Outline each blood parasite and name the species.
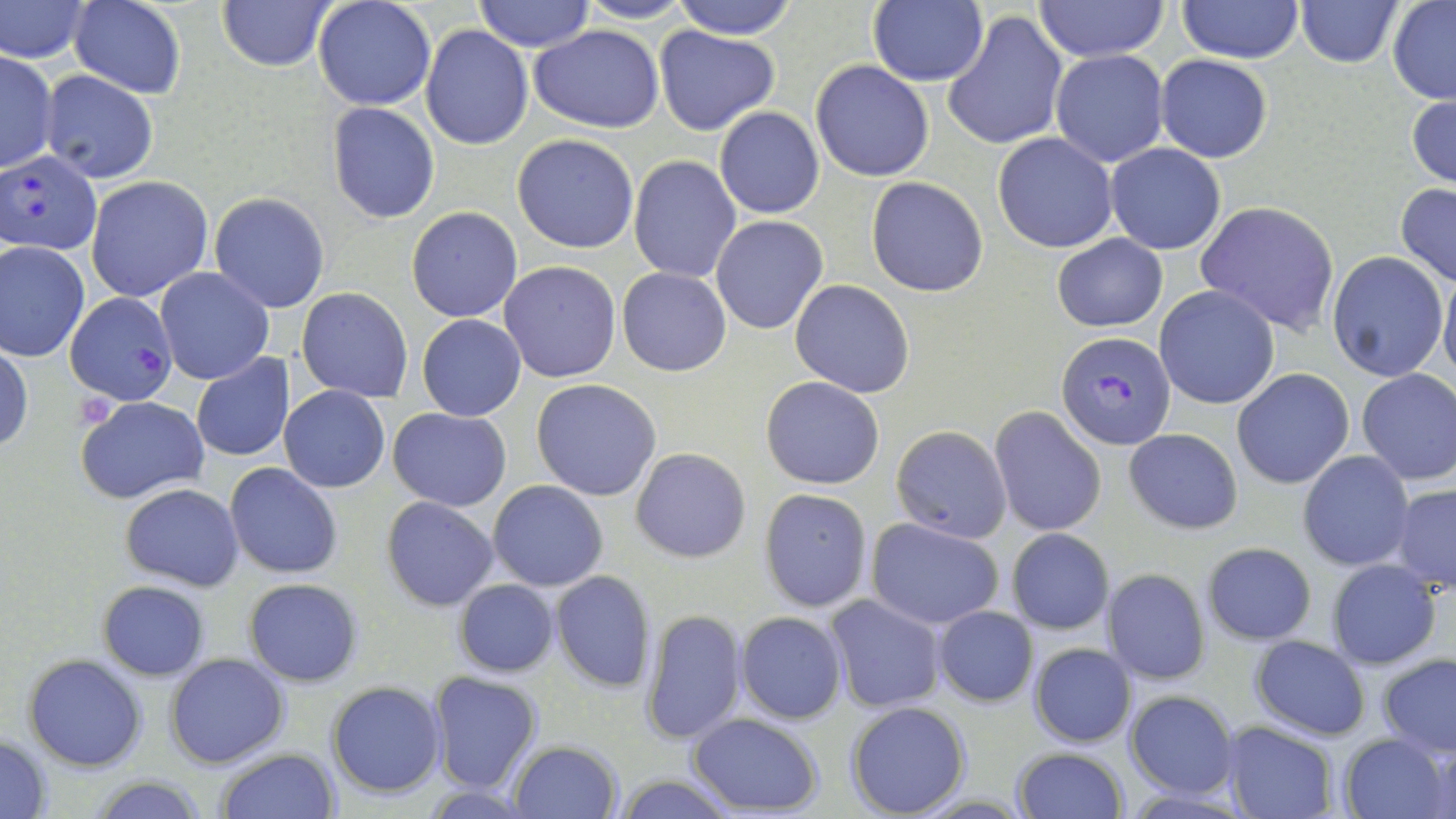
Approximate bounding boxes as (x1, y1, x2, y2) in pixels.
Plasmodium falciparum-infected red blood cells: (0, 150, 102, 255), (66, 292, 177, 406), (1057, 332, 1175, 450).
No Plasmodium ovale, Plasmodium malariae, Plasmodium vivax, Babesia divergens, or Trypanosoma brucei observed.

Uninfected red blood cell locations: (217, 0, 336, 73), (312, 0, 436, 110), (474, 0, 594, 52), (574, 0, 698, 23), (668, 0, 801, 40), (1296, 0, 1401, 68), (1386, 0, 1456, 104), (0, 1, 94, 62), (68, 1, 185, 97), (1032, 1, 1169, 63), (1177, 1, 1305, 63), (867, 2, 990, 87), (943, 10, 1068, 152), (422, 25, 534, 149), (529, 26, 664, 133), (655, 26, 779, 135), (1, 49, 58, 174), (1050, 50, 1170, 167), (1155, 54, 1272, 163), (810, 59, 935, 182), (40, 70, 160, 184), (1407, 89, 1456, 191), (326, 103, 440, 223), (714, 106, 824, 219), (512, 134, 640, 254), (992, 134, 1118, 253), (1106, 143, 1226, 254), (629, 155, 741, 283), (86, 176, 214, 303), (866, 176, 990, 296), (1395, 182, 1456, 287), (209, 193, 329, 312), (1194, 200, 1341, 335), (406, 206, 523, 322), (711, 215, 828, 335), (1169, 232, 1317, 397), (1053, 233, 1167, 332), (0, 240, 90, 361), (1326, 251, 1449, 382), (497, 261, 623, 383), (1439, 263, 1456, 384), (618, 266, 731, 377), (156, 267, 274, 385), (791, 279, 914, 397), (1154, 285, 1280, 409), (297, 287, 415, 403), (417, 314, 526, 421), (0, 343, 33, 455), (191, 355, 295, 462), (1356, 367, 1455, 487), (1232, 368, 1355, 489), (760, 376, 885, 489), (531, 379, 661, 501), (279, 386, 390, 492), (75, 394, 209, 505), (990, 406, 1107, 538), (387, 409, 512, 509), (890, 424, 1013, 543), (1124, 429, 1243, 534), (630, 447, 751, 562), (1298, 450, 1414, 572), (226, 463, 343, 580), (487, 480, 608, 592), (119, 482, 245, 591), (1389, 484, 1456, 595), (759, 489, 872, 612), (381, 496, 500, 612), (866, 518, 1003, 630), (1007, 528, 1114, 634), (1200, 542, 1316, 644), (1326, 559, 1442, 670), (1101, 568, 1211, 684), (550, 570, 656, 691), (242, 577, 364, 687), (453, 579, 559, 677), (97, 581, 209, 681), (824, 596, 946, 713), (933, 606, 1037, 707), (639, 608, 748, 744), (735, 611, 847, 724), (1250, 637, 1370, 740), (1027, 641, 1139, 748), (165, 652, 289, 767), (22, 654, 148, 771), (1379, 655, 1455, 757), (427, 670, 542, 793), (326, 680, 446, 799), (1124, 690, 1238, 799), (846, 700, 971, 818), (686, 712, 825, 815), (1221, 720, 1340, 818), (0, 733, 53, 817), (1340, 734, 1450, 819), (509, 741, 622, 819), (214, 746, 340, 819), (1011, 747, 1127, 819), (614, 774, 739, 818), (86, 775, 213, 818). Platelet locations: (75, 392, 119, 431). Slide-level diagnosis: Plasmodium falciparum. Single field of view. Thin blood smear. Light microscopy. Captured at 1000x magnification. Image is 1456×819 pixels. May-Grünwald-Giemsa-stained preparation.